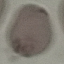

Summary:
  - Malaria status: uninfected
  - Capture: smartphone through the microscope eyepiece
  - Image type: automatically extracted cell patch, resized to 64 × 64 pixels
  - Stain: Giemsa
  - Preparation: thin blood film